Describe the morphology of the erythrocytes.
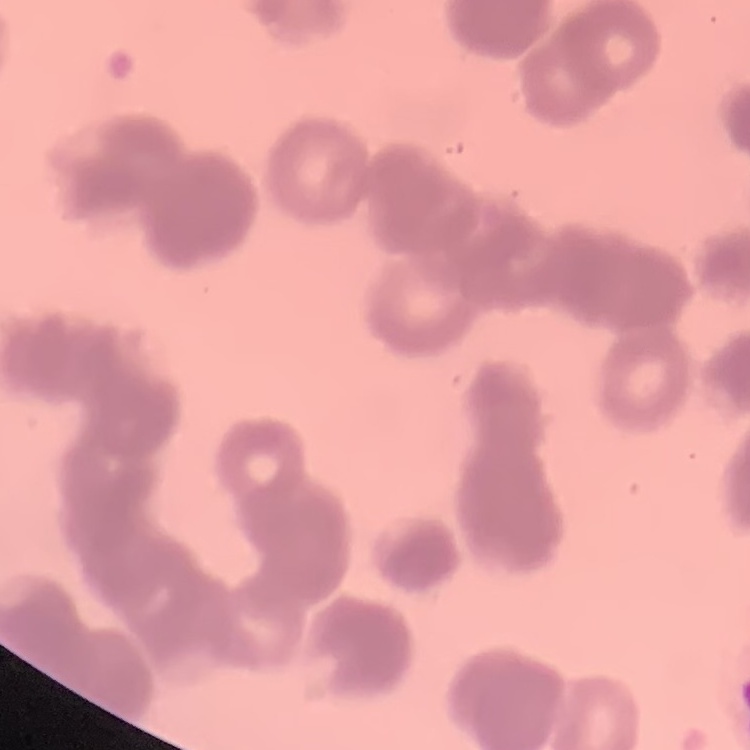
Rouleaux formation.

Summary:
  - Preparation: thin blood smear
  - Image type: one tile cut from a larger photomicrograph
  - Stain: Field's or Giemsa